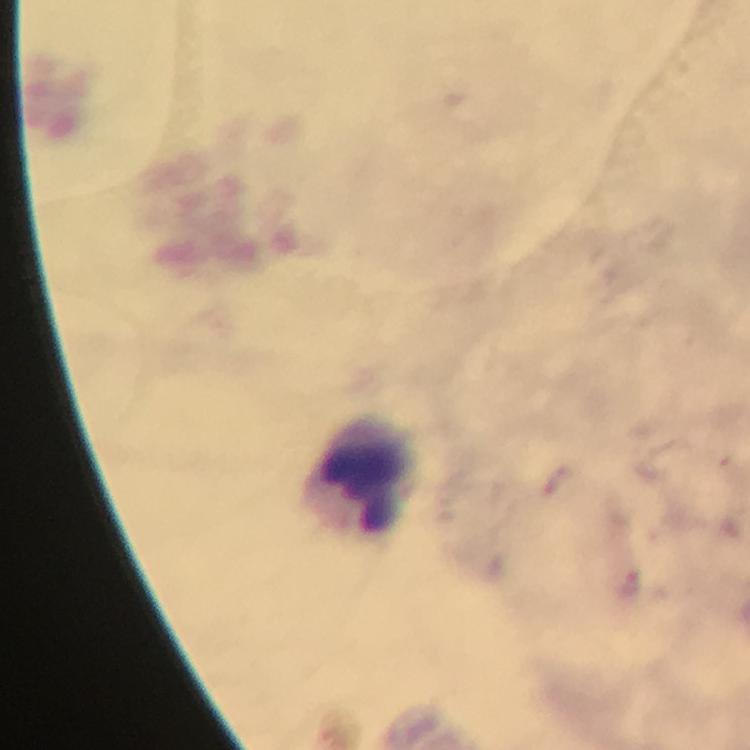 Approximate object centers, in pixels from the top-left corner. Plasmodium parasite locations: (x=632, y=585). Leukocyte locations: (x=365, y=471). A crop from one field of view. Thick blood smear. Immersion oil was used. Giemsa stain. Photographed with a smartphone mounted on the microscope. From a diagnostic examination for malaria. At 100x magnification. Image is 750×750 pixels.